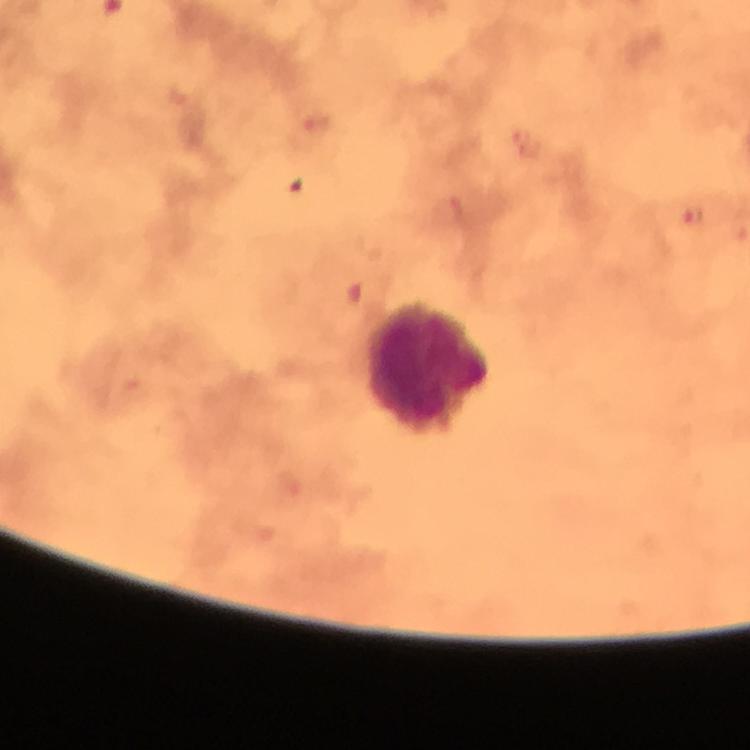
Approximate centers as {x, y} in pixels. Malaria parasite locations: {317, 124}, {694, 217}. Leukocyte locations: {429, 368}. Thick blood film. From a diagnostic examination for malaria. Giemsa-stained preparation. 100x magnification. Immersion oil applied. Photographed with a smartphone mounted on the microscope. Cropped region of a single field of view. Image is 750×750 pixels.